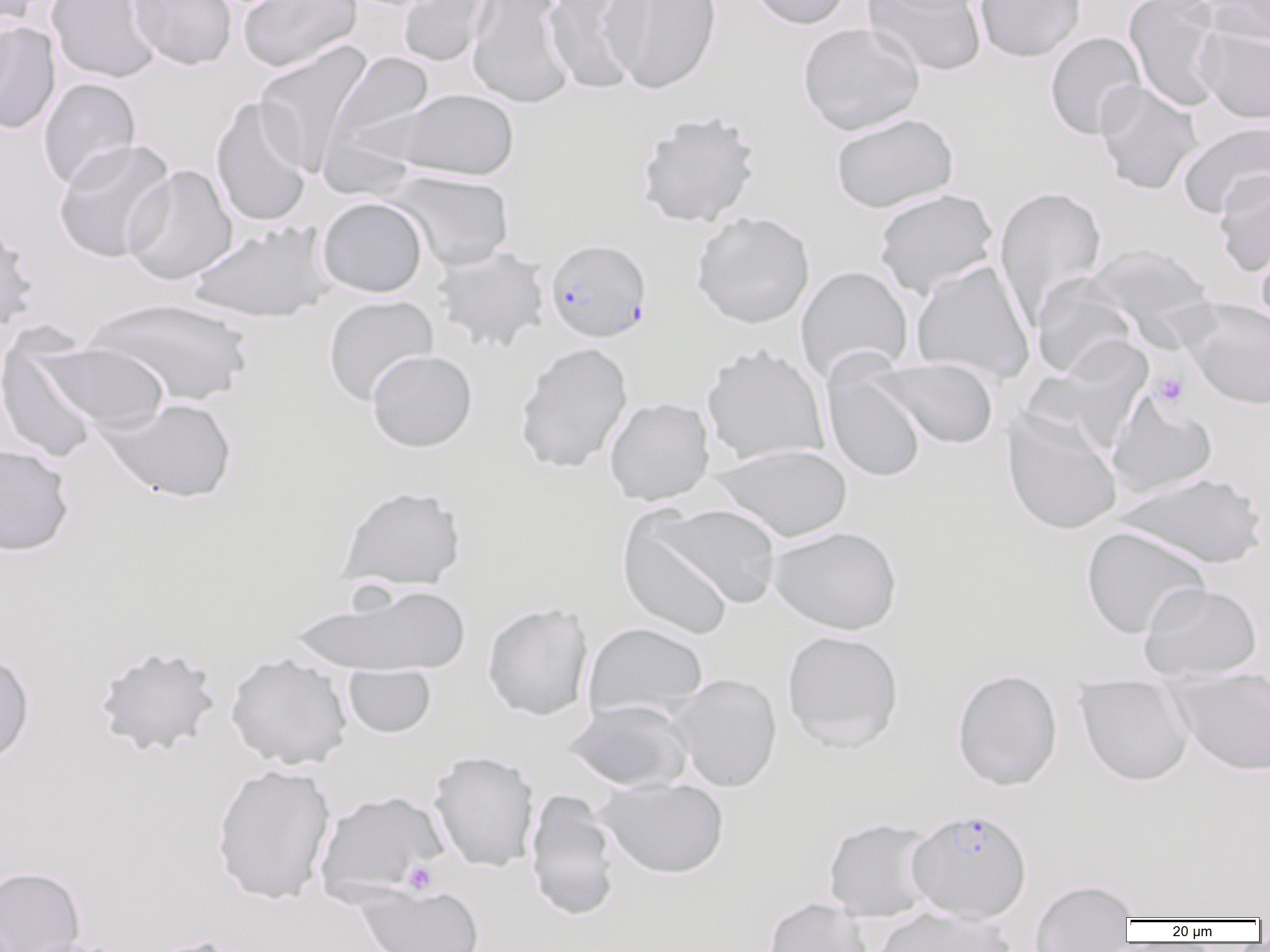
Approximate bounding boxes as named x1/y1/x2/y2 corners in pixels. Uninfected red blood cell locations: (x1=1, y1=0, x2=42, y2=36), (x1=45, y1=0, x2=162, y2=84), (x1=128, y1=0, x2=237, y2=71), (x1=237, y1=0, x2=362, y2=72), (x1=397, y1=0, x2=497, y2=68), (x1=466, y1=0, x2=576, y2=109), (x1=543, y1=0, x2=649, y2=94), (x1=602, y1=0, x2=722, y2=94), (x1=746, y1=0, x2=855, y2=30), (x1=862, y1=0, x2=988, y2=77), (x1=973, y1=0, x2=1086, y2=62), (x1=1123, y1=0, x2=1229, y2=111), (x1=1202, y1=0, x2=1270, y2=45), (x1=0, y1=20, x2=61, y2=134), (x1=798, y1=22, x2=925, y2=136), (x1=1195, y1=26, x2=1270, y2=124), (x1=1045, y1=31, x2=1146, y2=140), (x1=254, y1=42, x2=372, y2=174), (x1=327, y1=51, x2=436, y2=153), (x1=38, y1=77, x2=141, y2=190), (x1=1095, y1=81, x2=1203, y2=195), (x1=385, y1=88, x2=520, y2=181), (x1=210, y1=96, x2=313, y2=228), (x1=635, y1=111, x2=761, y2=228), (x1=830, y1=113, x2=958, y2=213), (x1=1177, y1=120, x2=1270, y2=219), (x1=52, y1=138, x2=176, y2=264), (x1=122, y1=164, x2=238, y2=285), (x1=386, y1=169, x2=515, y2=272), (x1=1213, y1=170, x2=1270, y2=278), (x1=994, y1=185, x2=1107, y2=326), (x1=873, y1=188, x2=999, y2=299), (x1=316, y1=197, x2=428, y2=298), (x1=691, y1=212, x2=815, y2=329), (x1=0, y1=218, x2=39, y2=333), (x1=187, y1=221, x2=335, y2=323), (x1=1255, y1=236, x2=1270, y2=330), (x1=1082, y1=243, x2=1214, y2=337), (x1=431, y1=246, x2=550, y2=353), (x1=911, y1=259, x2=1035, y2=384), (x1=795, y1=265, x2=914, y2=383), (x1=1031, y1=276, x2=1142, y2=380), (x1=322, y1=295, x2=439, y2=406), (x1=84, y1=297, x2=255, y2=407), (x1=1183, y1=298, x2=1270, y2=410), (x1=0, y1=331, x2=105, y2=465), (x1=40, y1=341, x2=169, y2=432), (x1=514, y1=342, x2=634, y2=473), (x1=701, y1=345, x2=830, y2=466), (x1=366, y1=349, x2=477, y2=453), (x1=871, y1=358, x2=998, y2=450), (x1=822, y1=361, x2=927, y2=483), (x1=1107, y1=391, x2=1218, y2=497), (x1=100, y1=397, x2=238, y2=503), (x1=604, y1=397, x2=715, y2=506), (x1=1002, y1=408, x2=1122, y2=536), (x1=0, y1=443, x2=74, y2=557), (x1=712, y1=443, x2=852, y2=542), (x1=1114, y1=472, x2=1268, y2=569), (x1=337, y1=485, x2=466, y2=591), (x1=650, y1=503, x2=782, y2=609), (x1=617, y1=513, x2=735, y2=640), (x1=768, y1=525, x2=903, y2=635), (x1=1081, y1=526, x2=1210, y2=639), (x1=1139, y1=581, x2=1263, y2=681), (x1=291, y1=582, x2=473, y2=677), (x1=481, y1=602, x2=593, y2=721), (x1=583, y1=622, x2=708, y2=722), (x1=781, y1=630, x2=904, y2=753), (x1=93, y1=644, x2=222, y2=757), (x1=0, y1=650, x2=35, y2=768), (x1=225, y1=652, x2=353, y2=770), (x1=342, y1=665, x2=437, y2=739), (x1=952, y1=669, x2=1063, y2=791), (x1=1168, y1=671, x2=1270, y2=775), (x1=670, y1=673, x2=782, y2=792), (x1=1075, y1=677, x2=1194, y2=785), (x1=565, y1=699, x2=693, y2=792), (x1=428, y1=750, x2=540, y2=873), (x1=210, y1=763, x2=336, y2=904), (x1=596, y1=777, x2=729, y2=878), (x1=314, y1=790, x2=448, y2=901), (x1=524, y1=792, x2=622, y2=920), (x1=823, y1=817, x2=938, y2=922), (x1=0, y1=865, x2=87, y2=952), (x1=1030, y1=879, x2=1138, y2=951), (x1=354, y1=884, x2=484, y2=952), (x1=762, y1=897, x2=872, y2=952), (x1=869, y1=905, x2=1017, y2=952), (x1=11, y1=936, x2=139, y2=952). Plasmodium falciparum-infected red blood cell locations: (x1=544, y1=238, x2=652, y2=343), (x1=906, y1=808, x2=1032, y2=923). Platelet locations: (x1=1152, y1=372, x2=1188, y2=407), (x1=402, y1=861, x2=437, y2=895). Slide-level diagnosis: Plasmodium falciparum. Thin blood film. Captured at 1000x magnification. Image is 1270×952 pixels. Optical microscopy. One field of a larger specimen.